Identify the blood parasite species.
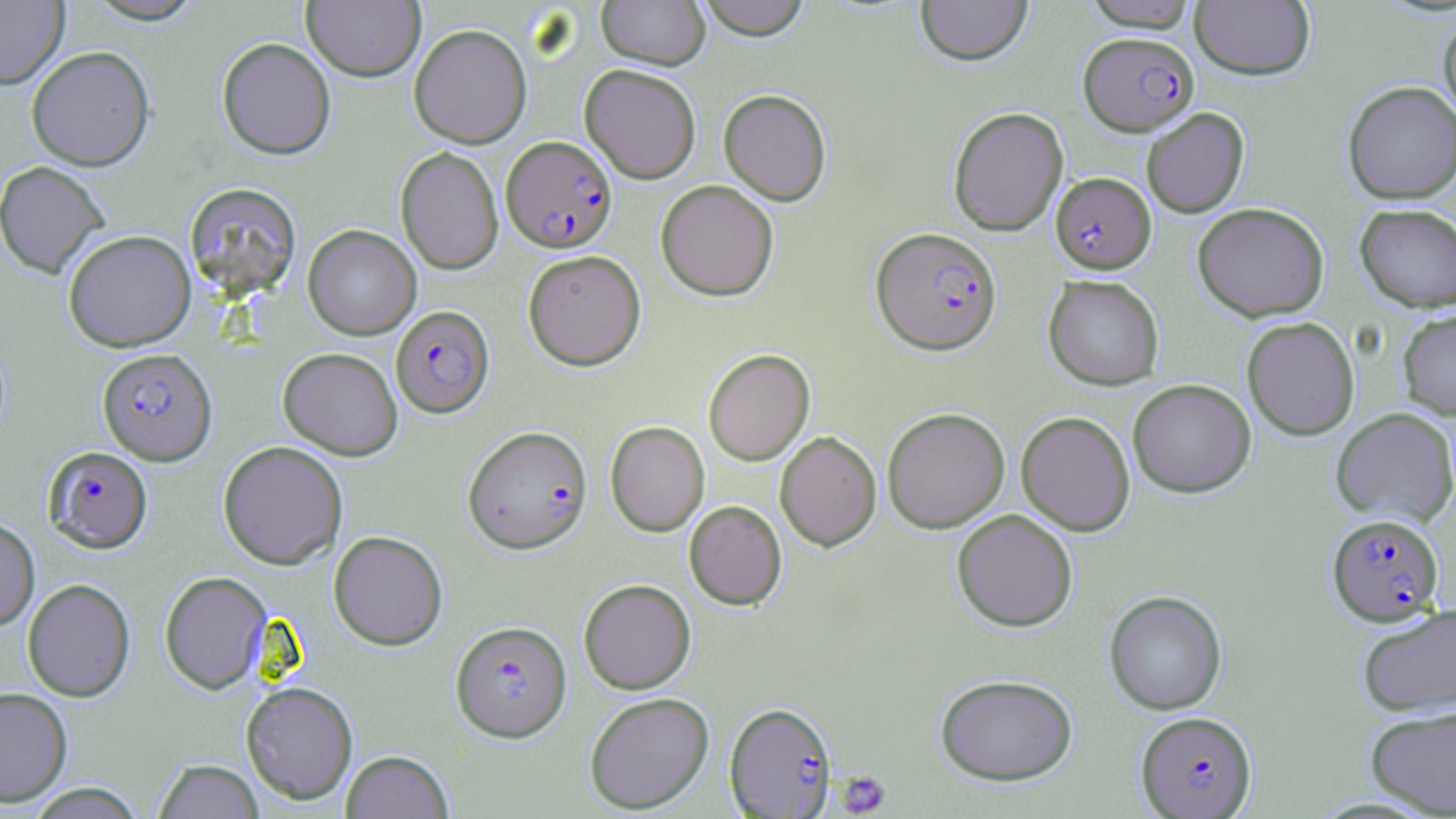
Plasmodium falciparum.

Summary:
  - Coordinate format: approximate bounding boxes as (x1,y1)-(x2,y2) corner pairs in pixels
  - Platelet locations: (836,771)-(892,816)
  - Plasmodium falciparum-infected red blood cell locations: (1080,32)-(1198,135), (501,135)-(618,253), (1051,172)-(1155,274), (872,227)-(1001,354), (391,305)-(494,417), (97,348)-(217,465), (464,426)-(592,553), (43,447)-(152,553), (1327,513)-(1445,626), (451,621)-(572,742), (724,701)-(838,817), (1136,711)-(1257,817)
  - Uninfected red blood cell locations: (0,0)-(69,89), (80,0)-(208,25), (695,0)-(812,40), (916,0)-(1032,65), (1081,0)-(1201,31), (302,1)-(425,81), (597,1)-(710,70), (1190,1)-(1315,80), (1438,14)-(1456,126), (405,24)-(517,273), (409,24)-(531,148), (217,37)-(336,160), (26,46)-(155,170), (580,64)-(701,183), (1342,81)-(1456,204), (718,89)-(832,205), (948,106)-(1069,235), (1142,107)-(1249,218), (395,147)-(503,275), (0,161)-(110,279), (656,180)-(779,301), (185,182)-(302,299), (1193,202)-(1329,321), (1355,203)-(1456,311), (303,225)-(421,340), (63,229)-(196,351), (523,249)-(646,370), (1043,275)-(1164,390), (1397,309)-(1456,419), (1242,317)-(1360,440), (278,347)-(402,459), (703,348)-(815,465), (1128,379)-(1256,497), (882,407)-(1010,533), (1331,408)-(1456,527), (1017,411)-(1135,536), (605,421)-(709,536), (775,431)-(881,551), (218,441)-(347,569), (684,501)-(786,610), (952,509)-(1077,631), (0,516)-(39,631), (329,530)-(448,650), (159,571)-(271,694), (23,578)-(135,701), (579,578)-(696,694), (1104,591)-(1227,715), (1358,604)-(1456,717), (935,673)-(1078,786), (241,681)-(358,804), (0,686)-(73,806), (584,692)-(714,813), (1365,704)-(1456,816), (340,750)-(454,819), (153,759)-(264,819), (23,784)-(148,819)
  - Preparation: thin blood film
  - Field of view: one of a larger specimen
  - Image size: 1456×819 pixels
  - Stain: May-Grünwald-Giemsa
  - Modality: light microscopy
  - Magnification: 1000x